Identify the parasite.
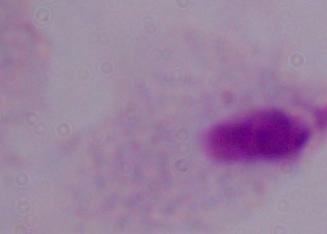

This is a trichomonad.

modality = micrograph
magnification = 1000x